Locate every Plasmodium ovale-infected red blood cell.
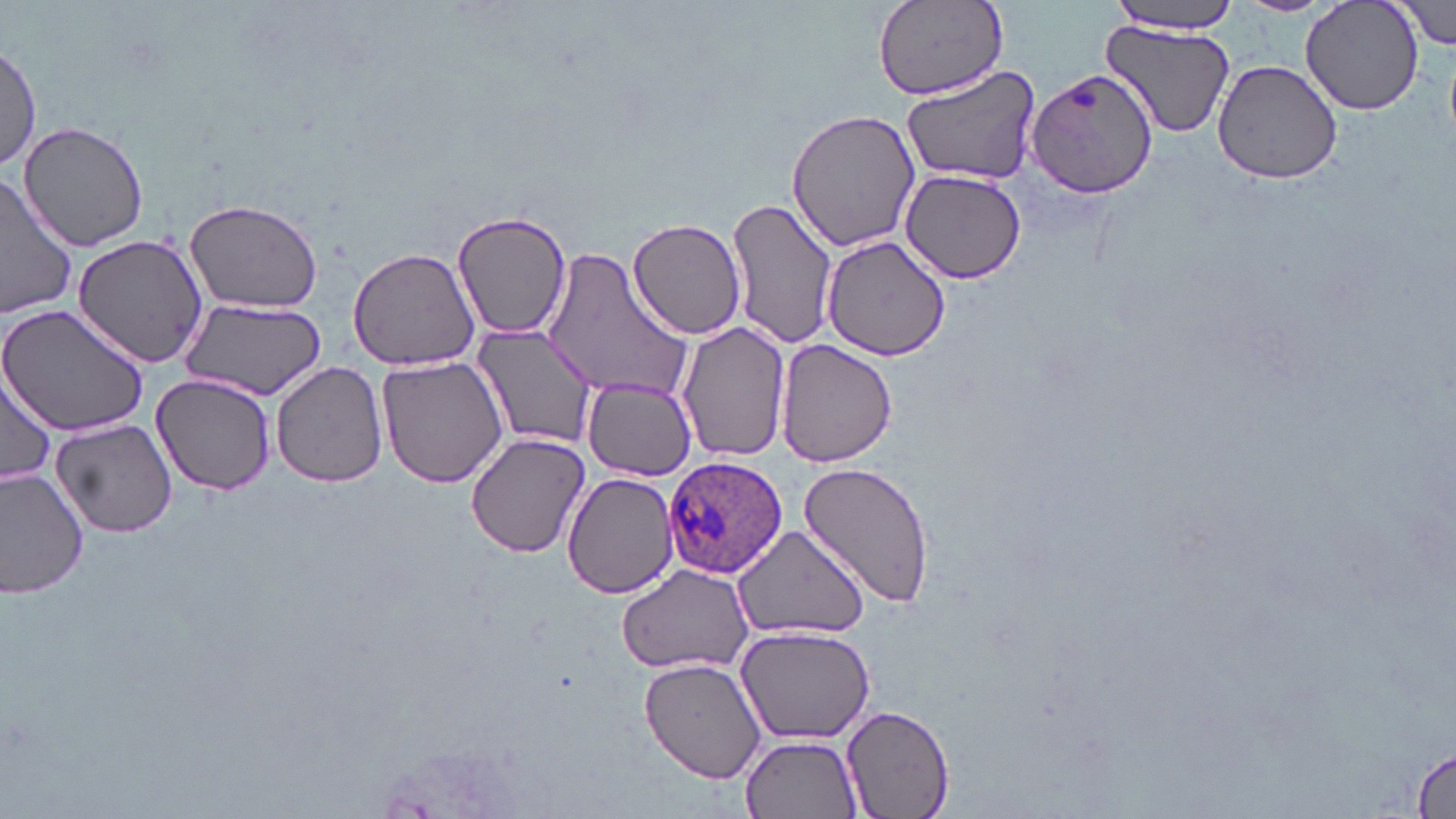
Approximate bounding boxes as [x1, y1, x2, y2] in pixels.
Plasmodium ovale-infected red blood cells: [663, 454, 788, 580].

slide-level diagnosis = Plasmodium ovale
magnification = 1000x
image size = 1456×819 pixels
stain = May-Grünwald-Giemsa
modality = optical microscopy
field of view = one of a larger specimen
uninfected red blood cell locations = approximate bounding boxes as [x1, y1, x2, y2] in pixels: [873, 0, 1008, 100], [1108, 0, 1242, 35], [1232, 0, 1334, 16], [1300, 0, 1425, 117], [1392, 0, 1454, 50], [1100, 22, 1236, 138], [1, 44, 41, 172], [1211, 60, 1344, 186], [902, 64, 1042, 186], [1027, 67, 1163, 200], [786, 108, 920, 254], [16, 119, 151, 252], [900, 170, 1028, 281], [1, 173, 79, 320], [726, 195, 841, 353], [185, 198, 323, 314], [451, 210, 573, 340], [627, 216, 746, 341], [70, 233, 211, 369], [820, 234, 951, 361], [347, 247, 481, 371], [543, 250, 692, 406], [180, 296, 326, 402], [0, 304, 151, 436], [676, 320, 792, 464], [475, 321, 598, 446], [774, 339, 900, 467], [378, 354, 509, 488], [271, 361, 388, 488], [1, 368, 58, 489], [152, 373, 276, 494], [584, 381, 695, 480], [51, 417, 178, 537], [466, 431, 590, 558], [799, 459, 936, 610], [0, 467, 91, 600], [562, 470, 680, 600], [616, 563, 754, 675], [734, 625, 878, 746], [638, 658, 770, 786], [838, 705, 958, 819], [742, 736, 861, 818], [1413, 745, 1453, 818]
preparation = thin blood smear